Name the parasite shown.
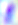

This is Toxoplasma gondii.

400x magnification. Photomicrograph.